Assess this cell for malaria.
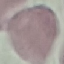

It is uninfected.

Summary:
  - Image type: automatically extracted cell patch, resized to 64 × 64 pixels
  - Stain: Giemsa
  - Preparation: thin smear
  - Capture: smartphone through the microscope eyepiece